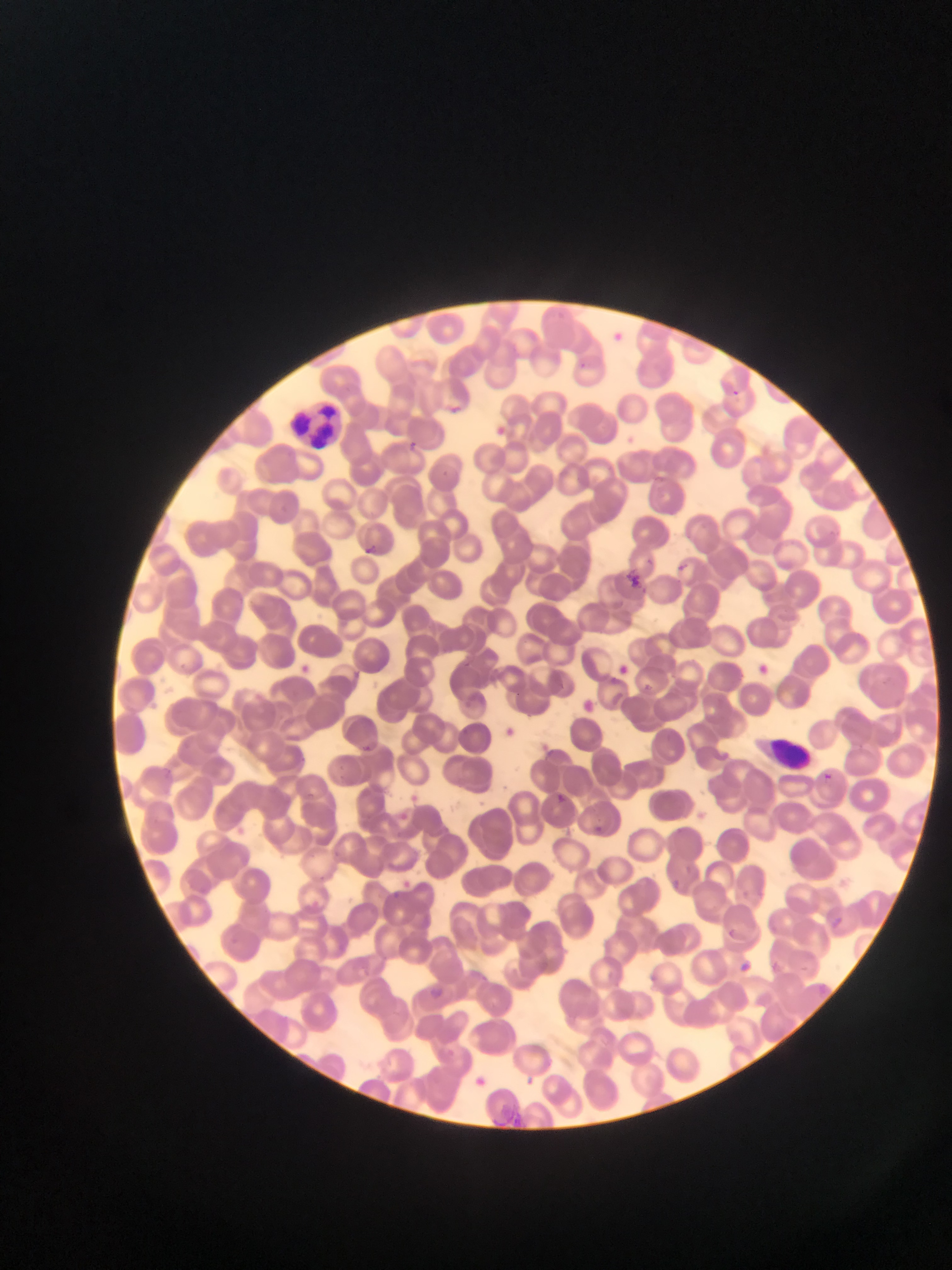

Approximate bounding boxes as [left, top, right, bottom] in pixels.
Summary:
  - Leukocyte locations: [293, 395, 348, 455], [759, 734, 809, 767]
  - Malaria parasite locations: [610, 327, 636, 348], [446, 401, 463, 415], [491, 421, 509, 437], [409, 433, 426, 455], [360, 535, 384, 557], [673, 558, 684, 569], [626, 567, 649, 594], [619, 659, 635, 686], [751, 659, 770, 679], [300, 664, 325, 679], [577, 697, 594, 719], [355, 737, 384, 764], [815, 771, 836, 782], [554, 784, 579, 812], [592, 821, 604, 836], [680, 860, 699, 877], [377, 888, 415, 900], [827, 912, 846, 935], [727, 926, 741, 939], [770, 958, 781, 973], [736, 959, 753, 977], [428, 981, 452, 996], [469, 1073, 486, 1085]
  - Image size: 952×1270 pixels
  - Preparation: thin blood film
  - Capture: mobile-phone photograph through a microscope
  - Country: Ghana
  - Field of view: single